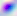

Micrograph. 400x magnification. Toxoplasma gondii is shown.